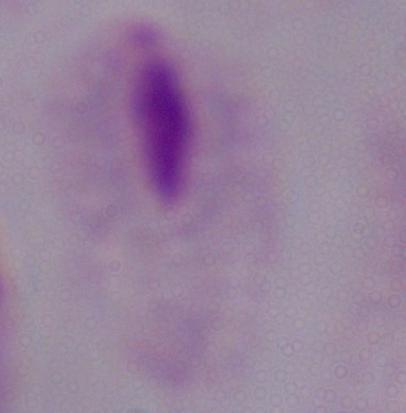

Photomicrograph. A trichomonad is shown. Captured at 1000x magnification.